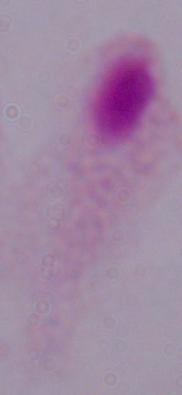 A trichomonad is seen. Captured at 1000x magnification. Photomicrograph.